Report the malaria status of this cell.
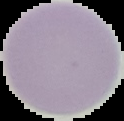

It is uninfected.

{
  "image_type": "cell region segmented out of the field of view; surrounding area masked to black",
  "image_size": "124×121 pixels",
  "preparation": "thin blood smear"
}